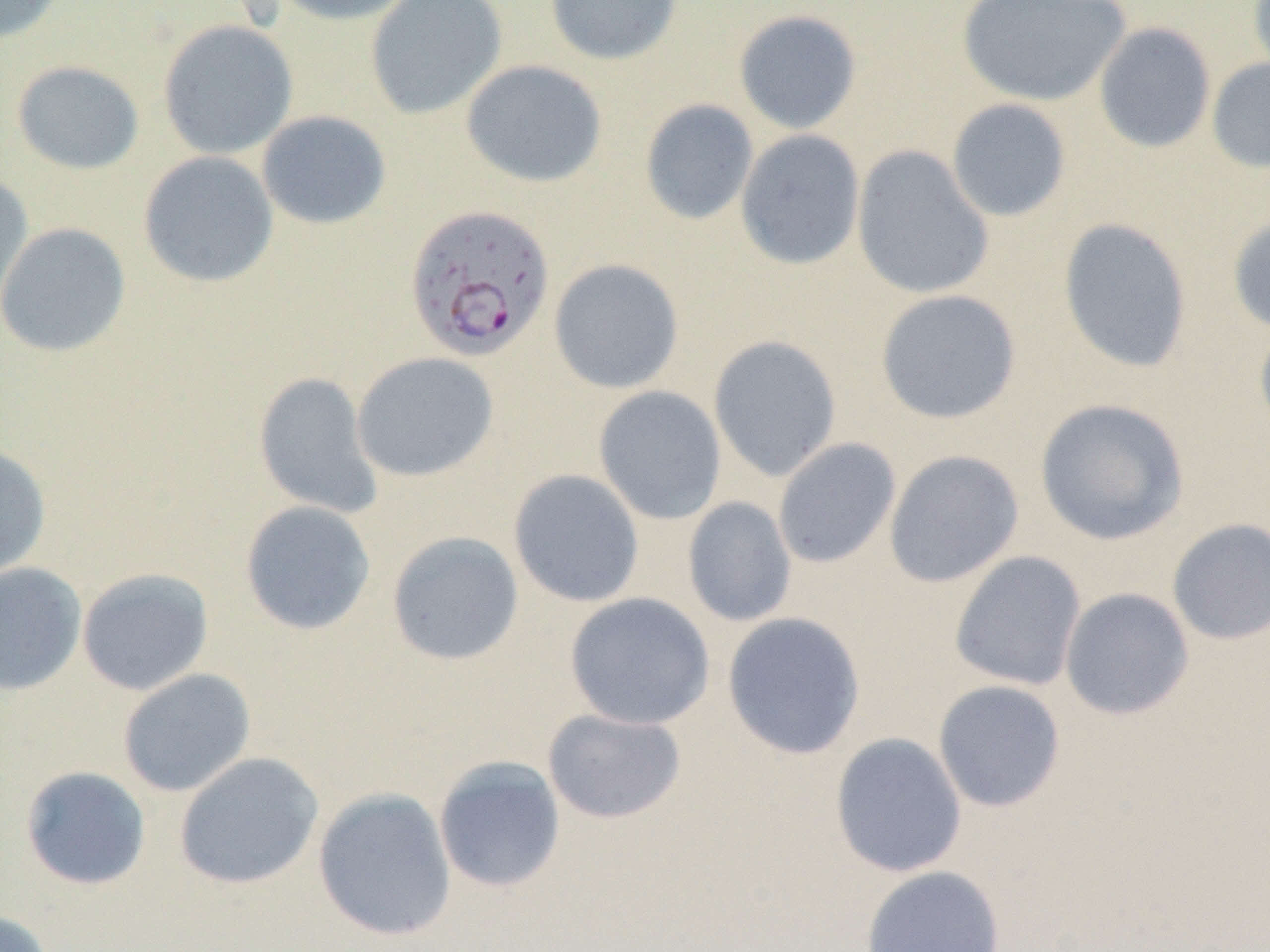

Approximate bounding boxes as named x1/y1/x2/y2 corners in pixels. Plasmodium falciparum-infected red blood cell locations: (x1=403, y1=202, x2=557, y2=362). Uninfected red blood cell locations: (x1=0, y1=0, x2=69, y2=45), (x1=268, y1=0, x2=419, y2=25), (x1=365, y1=0, x2=507, y2=119), (x1=544, y1=0, x2=684, y2=66), (x1=956, y1=0, x2=1131, y2=107), (x1=1247, y1=0, x2=1270, y2=81), (x1=733, y1=9, x2=863, y2=134), (x1=158, y1=20, x2=298, y2=159), (x1=1093, y1=22, x2=1216, y2=154), (x1=1206, y1=57, x2=1270, y2=174), (x1=11, y1=60, x2=145, y2=175), (x1=461, y1=60, x2=607, y2=188), (x1=946, y1=98, x2=1072, y2=222), (x1=639, y1=99, x2=759, y2=225), (x1=256, y1=110, x2=391, y2=229), (x1=735, y1=129, x2=865, y2=270), (x1=851, y1=145, x2=995, y2=300), (x1=138, y1=151, x2=279, y2=288), (x1=0, y1=172, x2=34, y2=322), (x1=1227, y1=211, x2=1270, y2=335), (x1=1057, y1=217, x2=1193, y2=373), (x1=0, y1=222, x2=132, y2=357), (x1=549, y1=258, x2=684, y2=393), (x1=875, y1=289, x2=1022, y2=424), (x1=1254, y1=315, x2=1270, y2=441), (x1=708, y1=335, x2=842, y2=481), (x1=351, y1=352, x2=499, y2=482), (x1=253, y1=371, x2=384, y2=519), (x1=592, y1=385, x2=728, y2=524), (x1=1034, y1=398, x2=1190, y2=546), (x1=773, y1=437, x2=901, y2=569), (x1=0, y1=440, x2=52, y2=583), (x1=884, y1=450, x2=1024, y2=588), (x1=508, y1=468, x2=645, y2=607), (x1=682, y1=496, x2=797, y2=627), (x1=239, y1=500, x2=376, y2=635), (x1=1167, y1=518, x2=1270, y2=645), (x1=386, y1=530, x2=524, y2=666), (x1=949, y1=551, x2=1087, y2=692), (x1=0, y1=561, x2=87, y2=696), (x1=77, y1=567, x2=214, y2=696), (x1=1059, y1=587, x2=1195, y2=721), (x1=564, y1=592, x2=715, y2=730), (x1=722, y1=612, x2=866, y2=760), (x1=117, y1=668, x2=256, y2=797), (x1=932, y1=679, x2=1066, y2=813), (x1=541, y1=708, x2=686, y2=824), (x1=829, y1=732, x2=968, y2=877), (x1=173, y1=752, x2=324, y2=890), (x1=433, y1=755, x2=567, y2=893), (x1=20, y1=765, x2=151, y2=890), (x1=313, y1=788, x2=457, y2=941), (x1=860, y1=864, x2=1006, y2=952), (x1=0, y1=909, x2=55, y2=952). Slide-level diagnosis: Plasmodium falciparum. Single field of view. Thin blood smear. Image is 1270×952 pixels. 1000x magnification. Light microscopy.